Identify the preparation type.
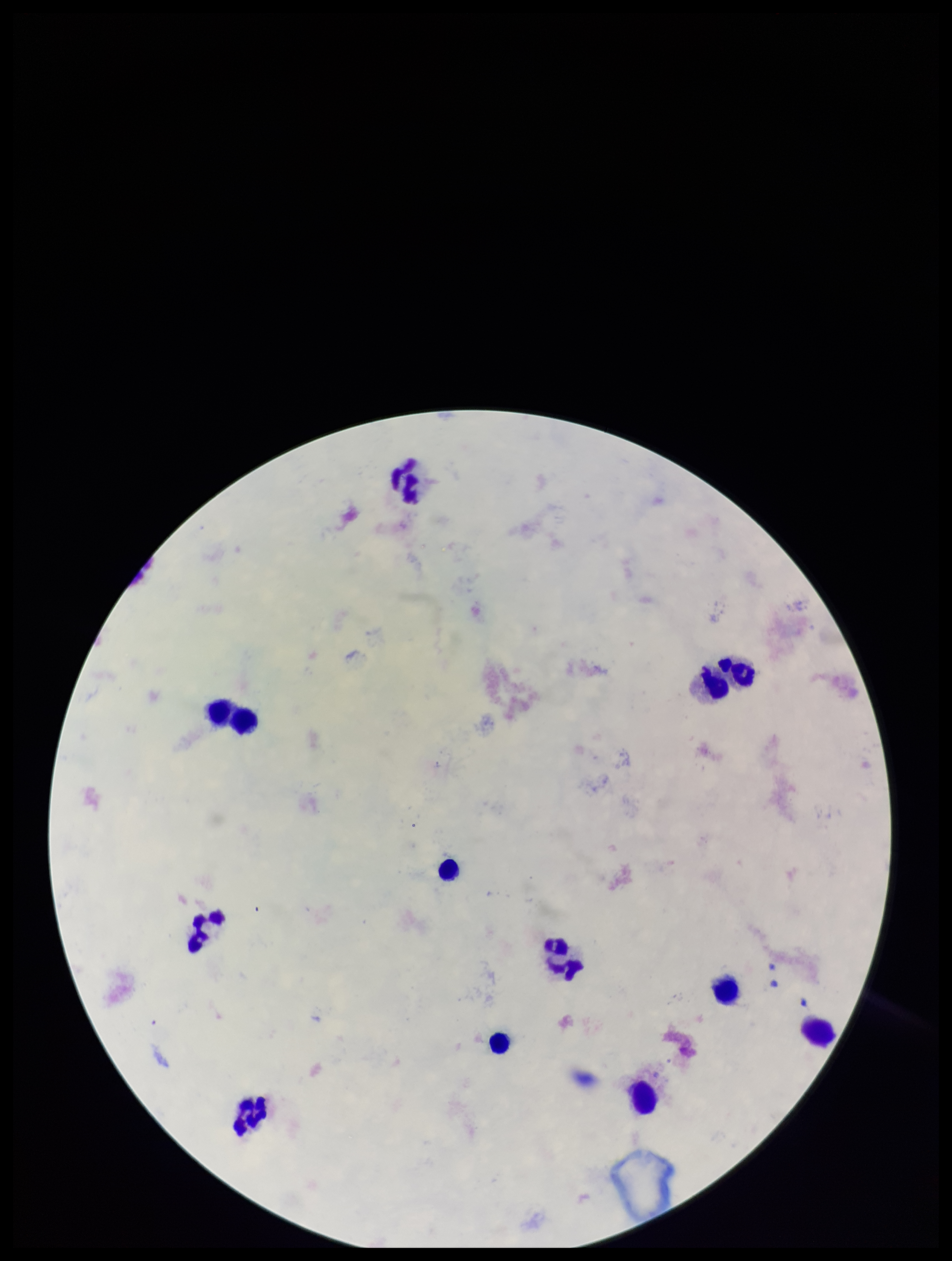

It is a thick blood smear.

Parasite count: 0. Plasmodium parasites: none identified. Giemsa stain. Image is 952×1261 pixels. Patient malaria status: negative. One field from this slide. Smartphone photograph taken through the eyepiece of a microscope. Leukocyte count: 12.